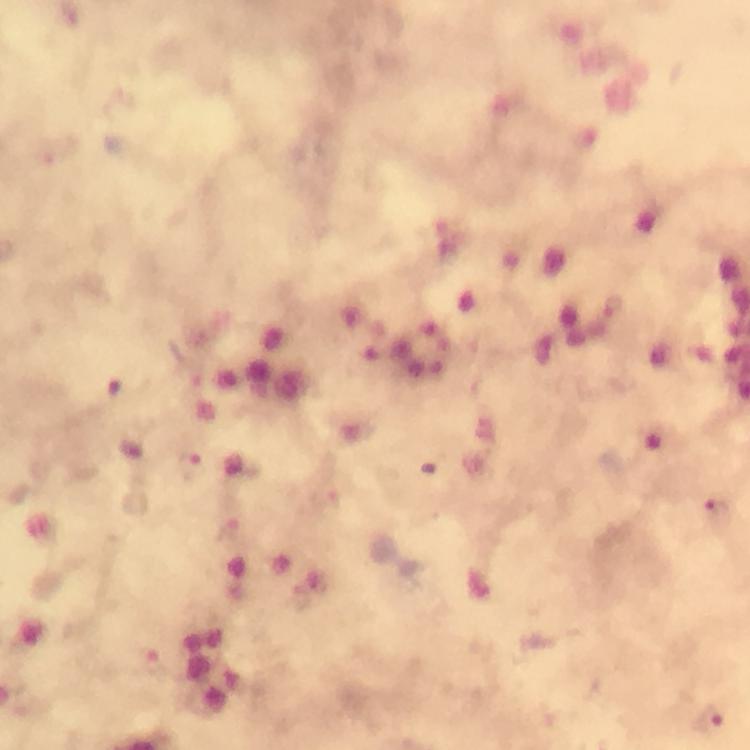

Approximate object centers, in pixels from the top-left corner.
Summary:
  - Plasmodium parasite locations: (x=614, y=307), (x=717, y=511), (x=708, y=717)
  - Stain: Giemsa
  - Preparation: thick smear
  - Capture: smartphone camera through the microscope
  - Cropped from: one field of view
  - Context: from a malaria diagnostic workup
  - Image size: 750×750 pixels
  - Magnification: 100x
  - Immersion oil: applied